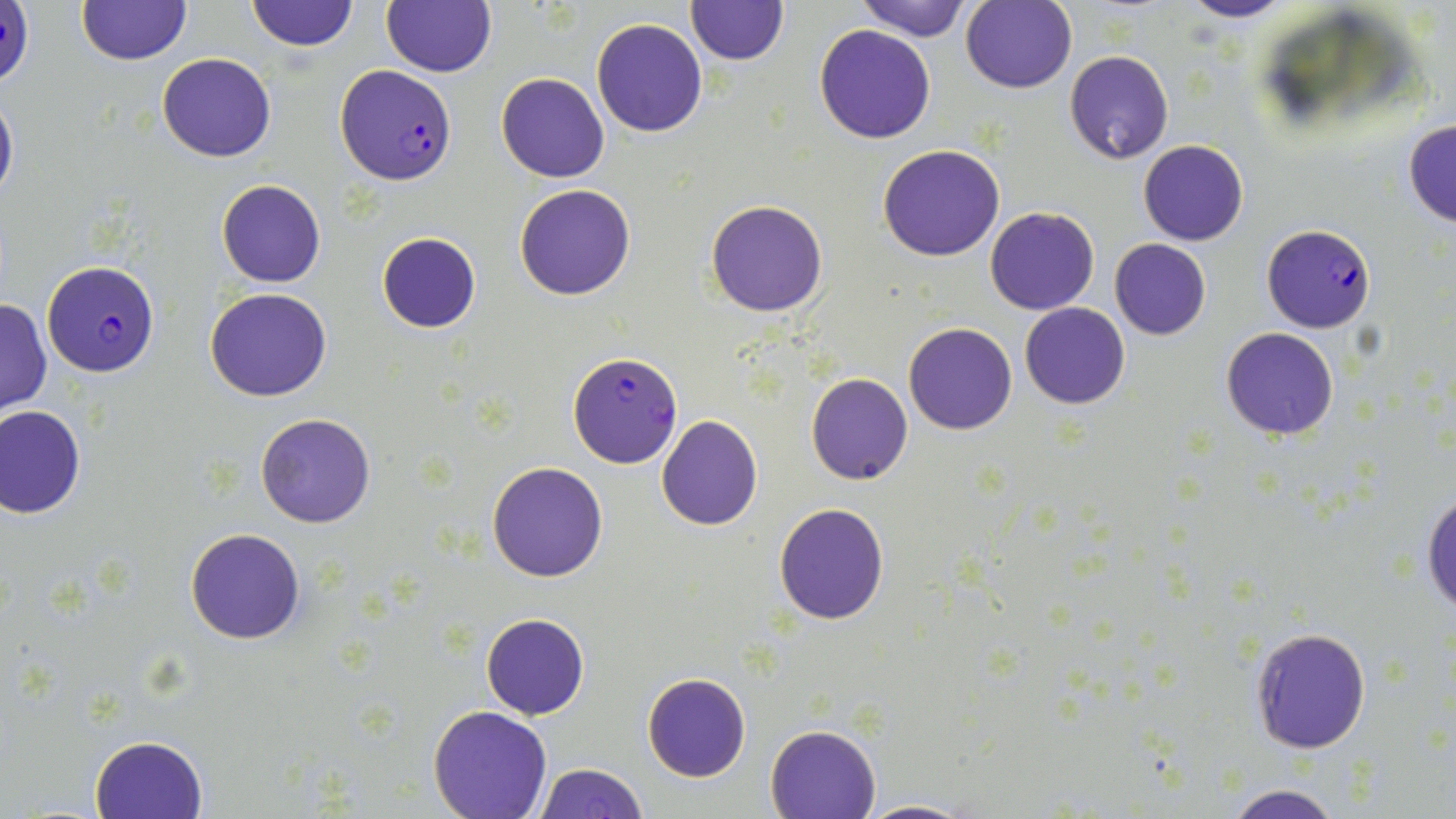
slide_level_diagnosis: Plasmodium falciparum
stain: May-Grünwald-Giemsa
image_size: 1456×819 pixels
field_of_view: single
modality: optical microscopy
uninfected_red_blood_cell_locations: 'approximate bounding boxes as [x1, y1, x2, y2] in pixels: [244, 0, 360, 53], [854, 0, 973, 41], [1178, 0, 1295, 23], [383, 1, 496, 77], [685, 1, 789, 67], [76, 2, 191, 66], [960, 2, 1077, 93], [592, 18, 707, 138], [814, 23, 936, 142], [1064, 49, 1173, 164], [156, 53, 276, 161], [496, 71, 610, 183], [0, 88, 19, 209], [1402, 119, 1456, 229], [1139, 139, 1249, 245], [877, 145, 1005, 262], [216, 178, 326, 287], [514, 183, 637, 301], [705, 200, 829, 317], [985, 207, 1098, 314], [376, 232, 481, 334], [1110, 239, 1211, 340], [206, 287, 330, 401], [0, 297, 52, 413], [1019, 302, 1130, 410], [903, 322, 1017, 434], [1220, 327, 1339, 440], [805, 372, 913, 485], [0, 404, 86, 519], [255, 412, 376, 528], [656, 415, 764, 530], [487, 461, 609, 582], [1421, 489, 1455, 620], [774, 502, 890, 624], [185, 528, 305, 645], [481, 612, 589, 720], [1249, 625, 1372, 755], [642, 673, 750, 782], [428, 706, 553, 819], [765, 724, 880, 818], [89, 733, 209, 818], [532, 762, 649, 819], [1217, 784, 1353, 819], [857, 798, 976, 818]'
preparation: thin blood film
magnification: 1000x
plasmodium_falciparum_infected_red_blood_cell_locations: 'approximate bounding boxes as [x1, y1, x2, y2] in pixels: [336, 64, 457, 185], [1261, 223, 1377, 333], [41, 260, 160, 376], [567, 353, 681, 468]'